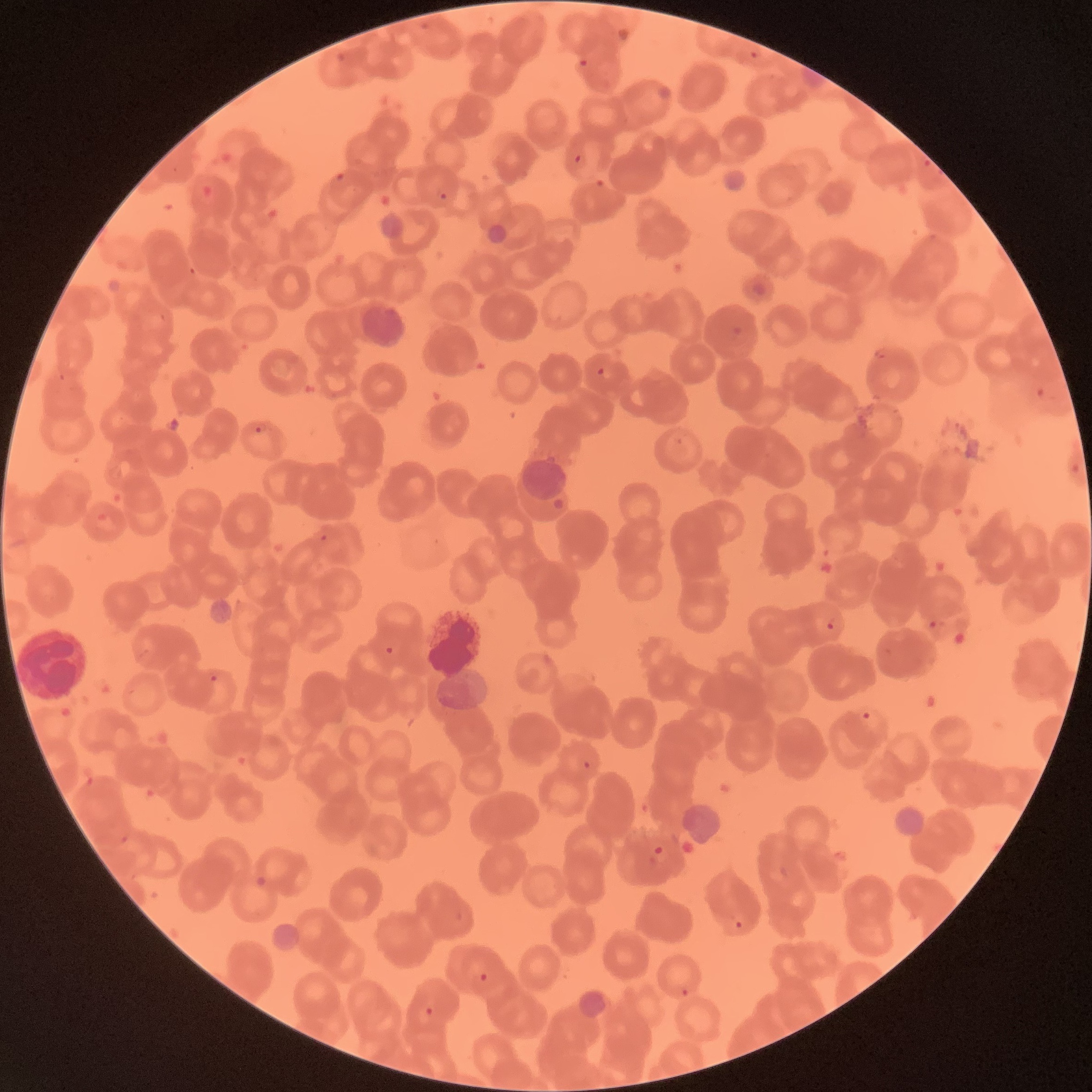

Approximate bounding boxes as named x1/y1/x2/y2 corners in pixels. White blood cell locations: (x1=14, y1=619, x2=90, y2=703). Plasmodium parasite locations: (x1=749, y1=50, x2=759, y2=59), (x1=335, y1=52, x2=347, y2=64), (x1=577, y1=58, x2=588, y2=68), (x1=573, y1=153, x2=582, y2=164), (x1=334, y1=172, x2=345, y2=181), (x1=436, y1=188, x2=449, y2=201), (x1=595, y1=366, x2=611, y2=380), (x1=253, y1=422, x2=268, y2=436), (x1=318, y1=533, x2=328, y2=543), (x1=825, y1=617, x2=836, y2=630), (x1=384, y1=645, x2=395, y2=657), (x1=209, y1=674, x2=219, y2=683), (x1=861, y1=711, x2=872, y2=721), (x1=582, y1=759, x2=592, y2=770), (x1=654, y1=844, x2=664, y2=857), (x1=734, y1=920, x2=743, y2=929), (x1=479, y1=973, x2=489, y2=983), (x1=680, y1=987, x2=690, y2=998), (x1=424, y1=1006, x2=434, y2=1016). Thin blood smear. Optical microscopy. The red blood cells show rouleaux formation. Image is 1092×1092 pixels.